Identify the parasite.
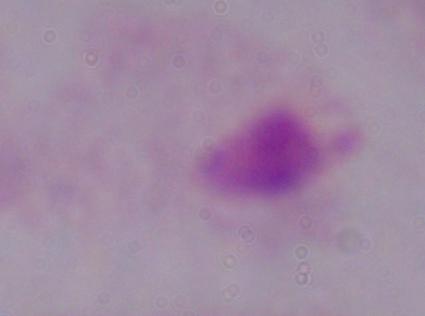

A trichomonad.

magnification: 1000x
modality: micrograph